Classify this cell by malaria status.
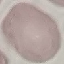

It is uninfected.

Summary:
  - Capture: smartphone through the microscope eyepiece
  - Preparation: thin blood smear
  - Image type: automatically extracted cell patch, resized to 64 × 64 pixels
  - Stain: Giemsa